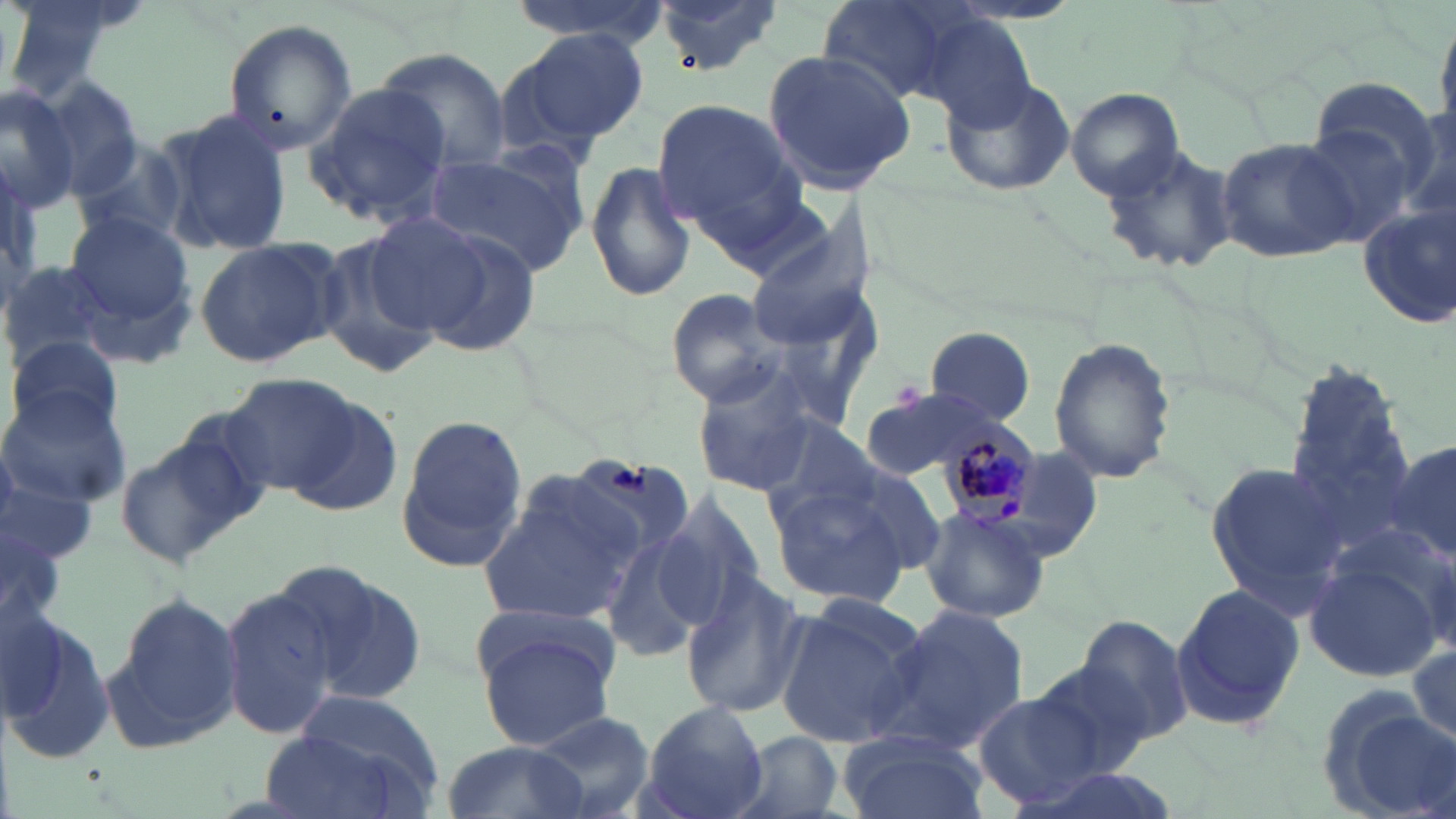 Approximate bounding boxes as named x1/y1/x2/y2 corners in pixels. Plasmodium malariae-infected red blood cell locations: (x1=936, y1=415, x2=1042, y2=534). Uninfected red blood cell locations: (x1=5, y1=0, x2=142, y2=98), (x1=507, y1=0, x2=672, y2=49), (x1=652, y1=0, x2=779, y2=77), (x1=817, y1=0, x2=983, y2=106), (x1=1430, y1=9, x2=1456, y2=134), (x1=920, y1=16, x2=1038, y2=132), (x1=222, y1=17, x2=357, y2=154), (x1=498, y1=26, x2=650, y2=154), (x1=371, y1=47, x2=512, y2=173), (x1=760, y1=48, x2=918, y2=193), (x1=939, y1=74, x2=1079, y2=196), (x1=35, y1=76, x2=147, y2=196), (x1=304, y1=80, x2=453, y2=227), (x1=1311, y1=80, x2=1440, y2=189), (x1=0, y1=83, x2=79, y2=209), (x1=1067, y1=87, x2=1182, y2=199), (x1=648, y1=98, x2=803, y2=236), (x1=154, y1=110, x2=294, y2=257), (x1=1298, y1=120, x2=1421, y2=250), (x1=1215, y1=136, x2=1359, y2=264), (x1=72, y1=138, x2=187, y2=247), (x1=1098, y1=142, x2=1239, y2=275), (x1=423, y1=147, x2=588, y2=279), (x1=585, y1=159, x2=698, y2=305), (x1=1355, y1=202, x2=1456, y2=328), (x1=744, y1=207, x2=876, y2=345), (x1=65, y1=213, x2=196, y2=351), (x1=362, y1=214, x2=498, y2=334), (x1=416, y1=229, x2=544, y2=357), (x1=311, y1=232, x2=445, y2=383), (x1=194, y1=233, x2=346, y2=368), (x1=2, y1=257, x2=116, y2=370), (x1=665, y1=288, x2=791, y2=408), (x1=922, y1=328, x2=1038, y2=424), (x1=1047, y1=335, x2=1177, y2=485), (x1=7, y1=336, x2=125, y2=443), (x1=1282, y1=357, x2=1419, y2=548), (x1=691, y1=365, x2=824, y2=496), (x1=222, y1=375, x2=362, y2=496), (x1=862, y1=387, x2=1015, y2=480), (x1=0, y1=392, x2=133, y2=508), (x1=278, y1=393, x2=404, y2=516), (x1=397, y1=411, x2=532, y2=573), (x1=758, y1=414, x2=882, y2=529), (x1=114, y1=430, x2=256, y2=572), (x1=1385, y1=433, x2=1456, y2=571), (x1=1205, y1=458, x2=1354, y2=613), (x1=834, y1=462, x2=951, y2=578), (x1=0, y1=464, x2=105, y2=567), (x1=477, y1=470, x2=649, y2=623), (x1=769, y1=482, x2=915, y2=608), (x1=651, y1=491, x2=768, y2=626), (x1=919, y1=504, x2=1052, y2=625), (x1=0, y1=516, x2=62, y2=647), (x1=601, y1=527, x2=716, y2=664), (x1=1301, y1=542, x2=1452, y2=687), (x1=279, y1=560, x2=427, y2=706), (x1=679, y1=569, x2=808, y2=720), (x1=1169, y1=582, x2=1305, y2=731), (x1=222, y1=583, x2=345, y2=738), (x1=808, y1=591, x2=928, y2=675), (x1=104, y1=592, x2=247, y2=748), (x1=774, y1=603, x2=919, y2=748), (x1=882, y1=606, x2=1029, y2=754), (x1=3, y1=609, x2=114, y2=767), (x1=1075, y1=615, x2=1198, y2=747), (x1=472, y1=620, x2=618, y2=752), (x1=1408, y1=632, x2=1456, y2=753), (x1=1027, y1=654, x2=1162, y2=778), (x1=1318, y1=688, x2=1449, y2=819), (x1=972, y1=689, x2=1109, y2=808), (x1=286, y1=690, x2=447, y2=808), (x1=637, y1=701, x2=768, y2=819), (x1=529, y1=710, x2=657, y2=819), (x1=259, y1=729, x2=408, y2=819), (x1=730, y1=730, x2=845, y2=819), (x1=839, y1=732, x2=985, y2=819), (x1=441, y1=740, x2=591, y2=819). Slide-level diagnosis: Plasmodium malariae. 1000x magnification. Thin blood smear. May-Grünwald-Giemsa stain. One field of a larger specimen. Light microscopy. Image is 1456×819 pixels.